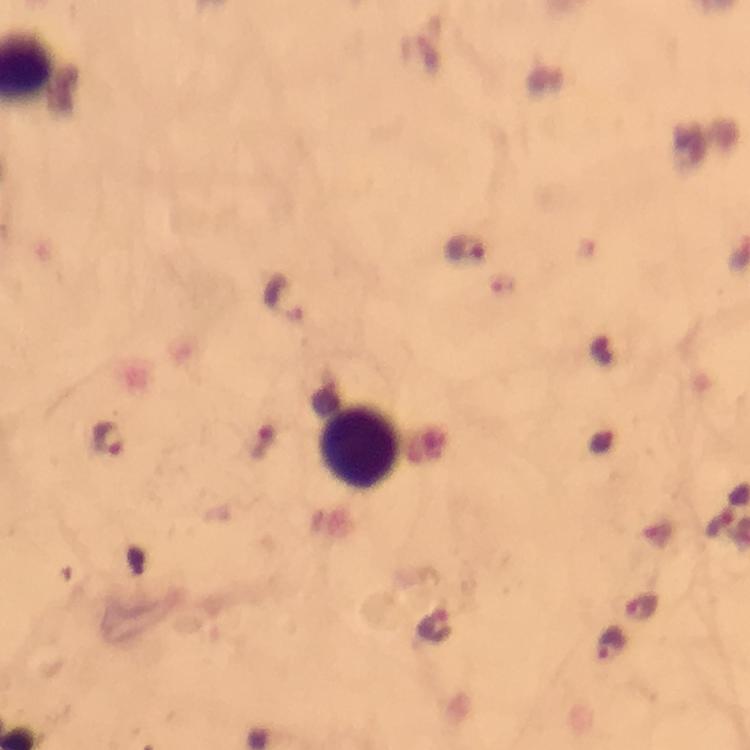
{
  "context": "from a malaria diagnostic workup",
  "immersion_oil": "used",
  "capture": "smartphone mounted on the microscope",
  "malaria_parasite_locations": "approximate centers as [x, y] in pixels: [465, 249], [285, 300], [108, 439], [641, 606], [434, 625], [611, 645]",
  "magnification": "100x",
  "image_size": "750×750 pixels",
  "leukocyte_locations": "approximate centers as [x, y] in pixels: [357, 449]",
  "stain": "Giemsa",
  "preparation": "thick blood smear",
  "cropped_from": "a single field of view"
}